Assess this cell for malaria.
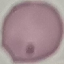
Uninfected.

Summary:
  - Stain: Giemsa
  - Capture: smartphone camera at the microscope eyepiece
  - Preparation: thin blood smear
  - Image type: automatically extracted cell patch, resized to 64 × 64 pixels